Report the malaria status.
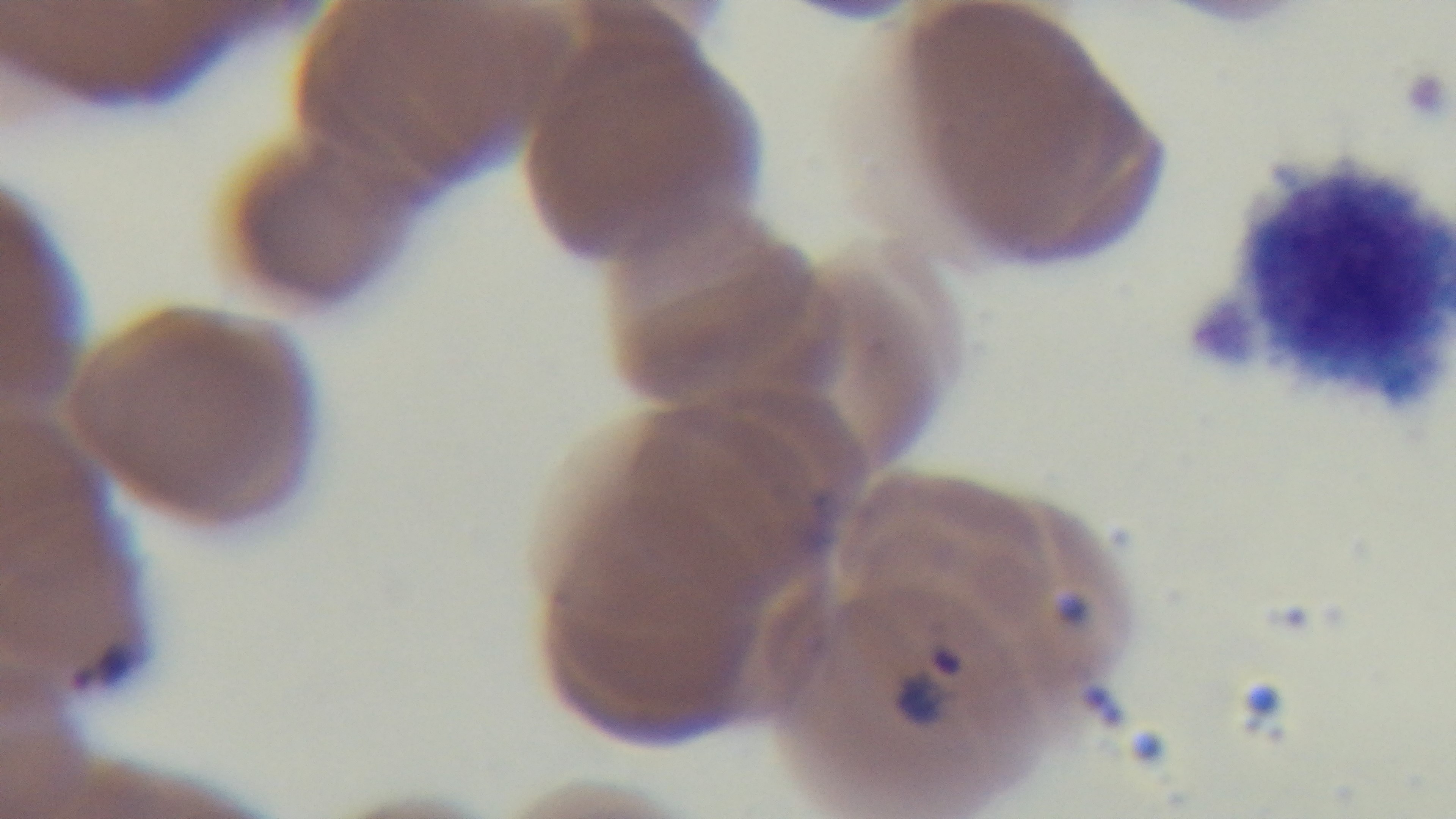

It is infected.

Giemsa-stained. One field from the slide. 100x oil-immersion objective. Preparation: thin smear. Light microscopy. Captured with a mounted 4K digital camera.